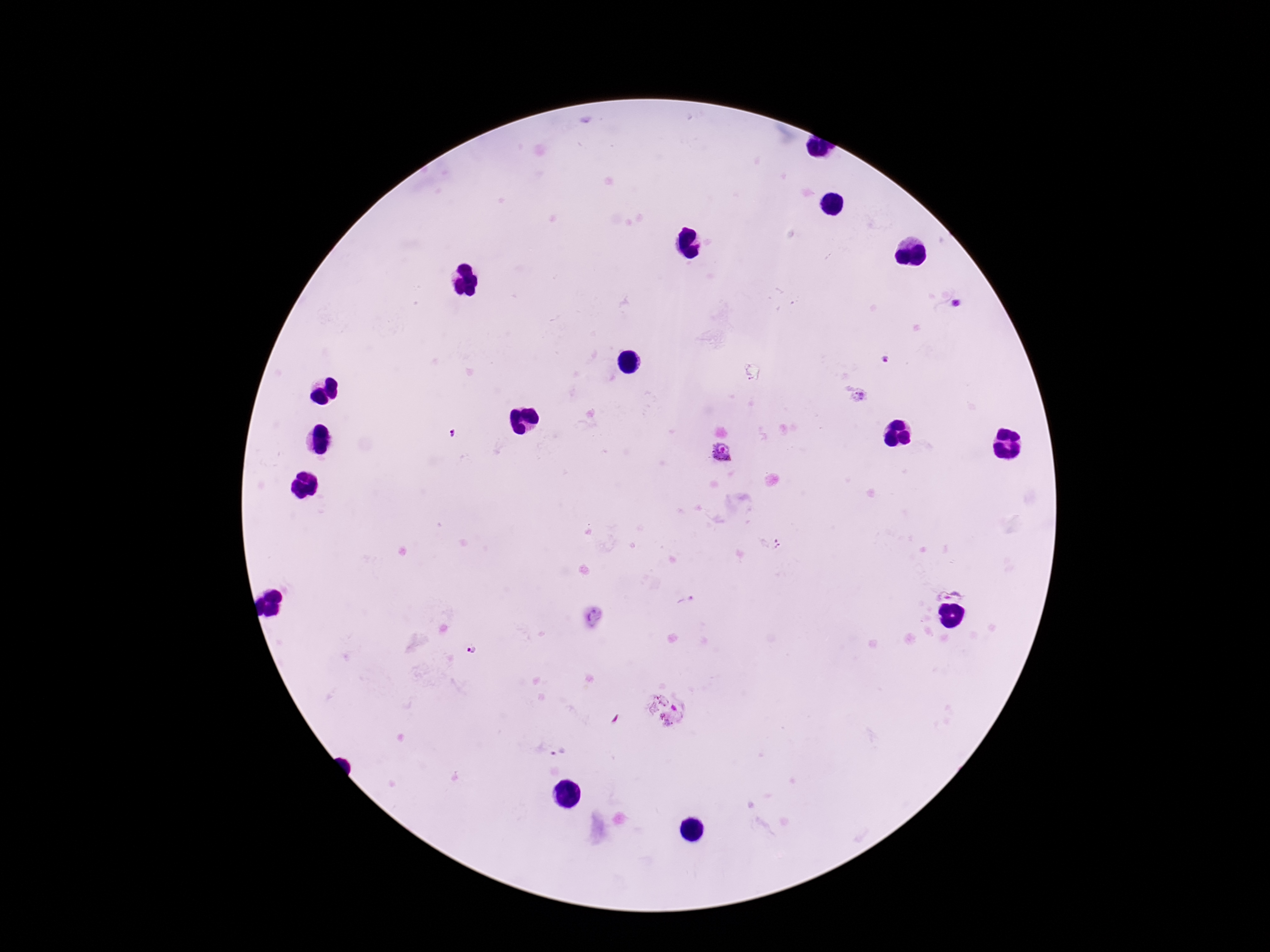 Approximate centers as (x, y) in pixels. Plasmodium parasite locations: (958, 303), (886, 359), (860, 397), (453, 434), (723, 452), (949, 587), (471, 651), (672, 710). 100x magnification. Patient malaria status: positive. Image is 1270×952 pixels. One field from this slide. Photographed through the microscope eyepiece with a smartphone camera. Thick peripheral-blood smear. Giemsa-stained preparation.